Comment on the morphology of the erythrocytes.
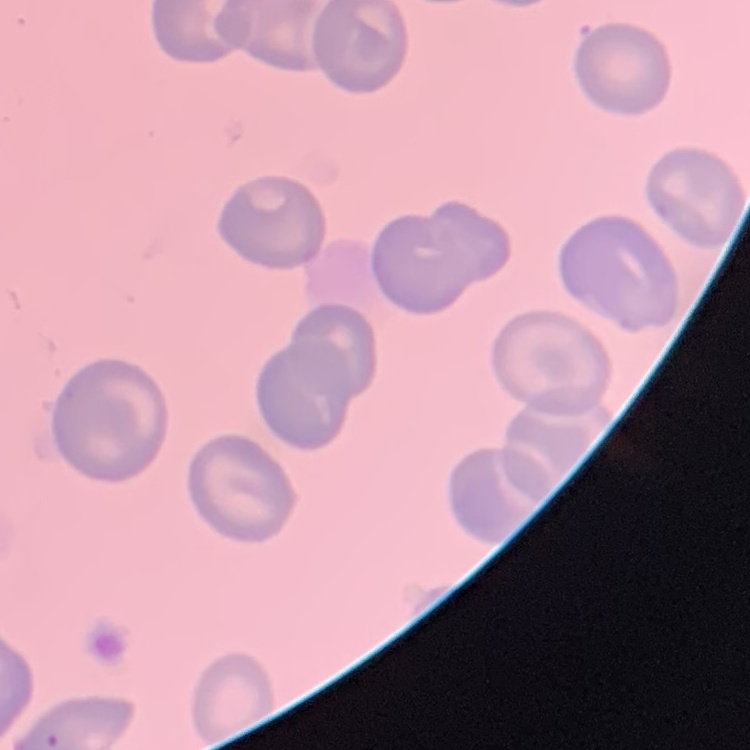

They show no rouleaux formation.

Summary:
  - Preparation: thin blood film
  - Image type: one tile cut from a larger photomicrograph
  - Stain: Field's or Giemsa